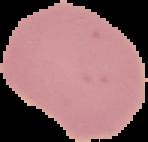

Summary:
  - Image type: segmented cell region with the area outside set to black
  - Image size: 148×142 pixels
  - Preparation: thin blood film
  - Result: no Plasmodium parasites detected